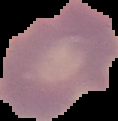

Segmented cell region on a black background. From a thin blood film. Result: negative for Plasmodium parasites. Image is 118×121 pixels.